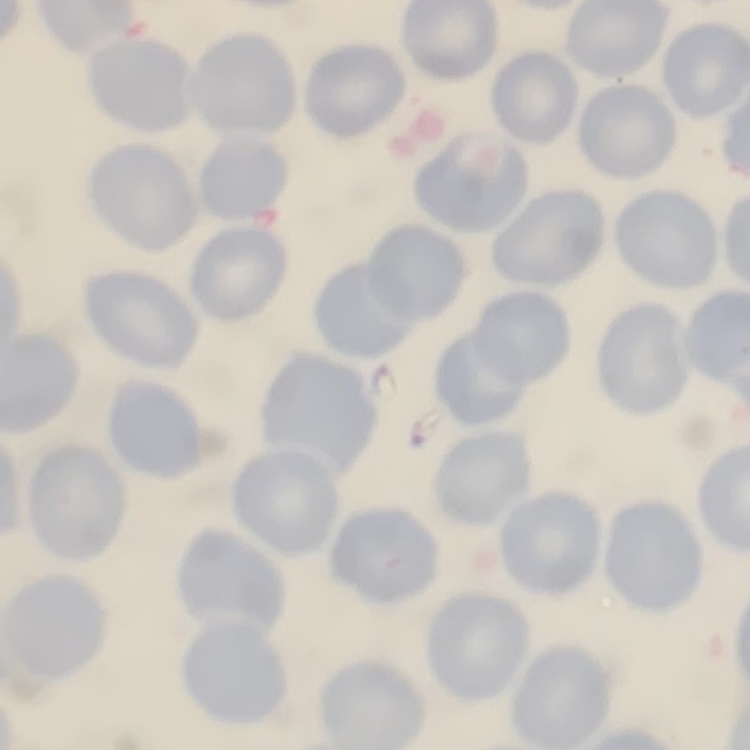

The erythrocytes exhibit no rouleaux formation. One tile cut from a larger photomicrograph. Field's or Giemsa stain. Thin blood smear.